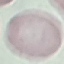

malaria status = uninfected
image type = cell patch, automatically extracted from a larger field of view and resized to 64 × 64 pixels
capture = smartphone through the microscope eyepiece
stain = Giemsa
preparation = thin blood smear